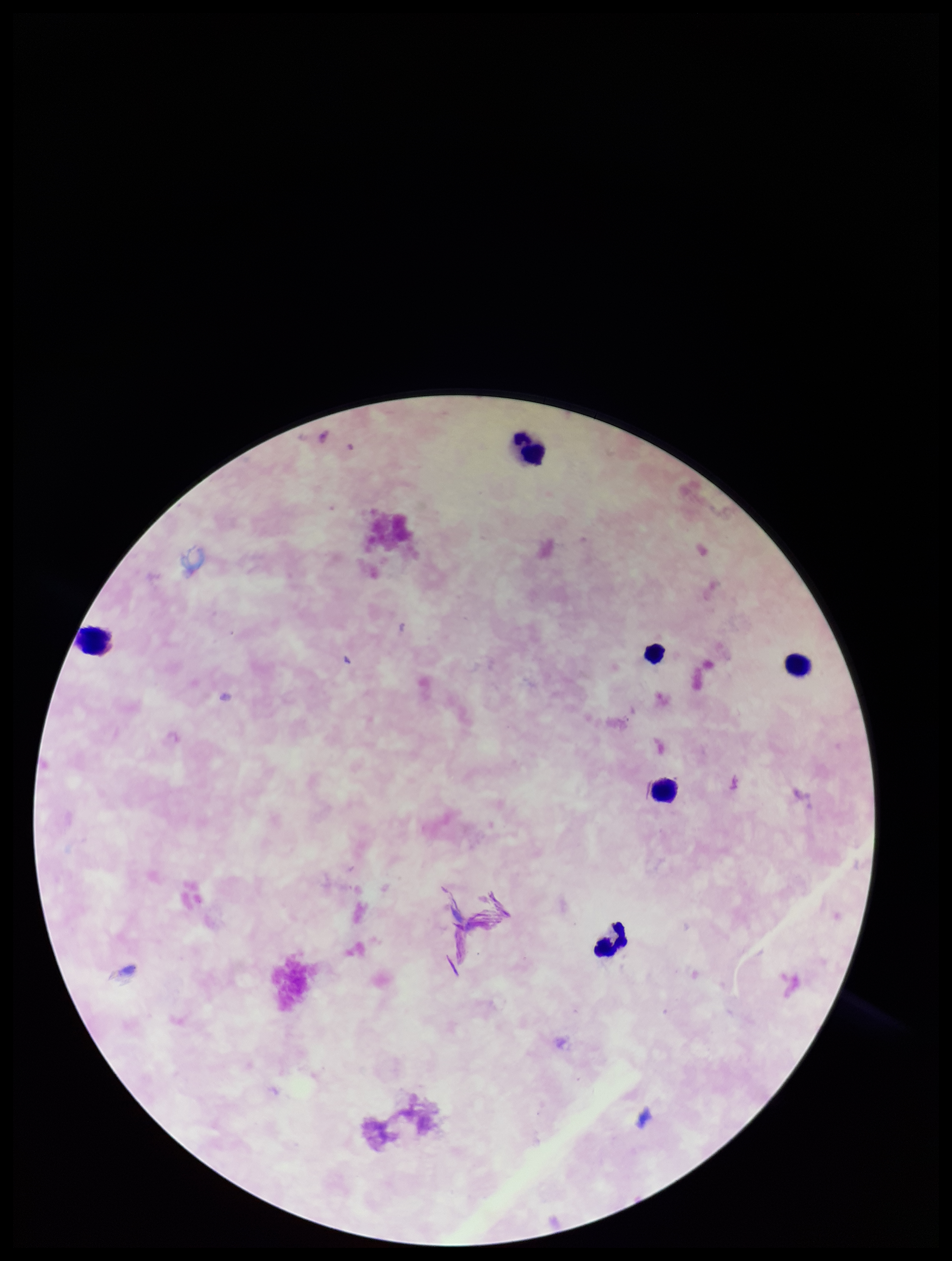

{
  "image_size": "952×1261 pixels",
  "field_of_view": "one from this slide",
  "parasite_count": 0,
  "patient_malaria_status": "negative",
  "capture": "smartphone photograph through the microscope eyepiece",
  "preparation": "thick",
  "stain": "Giemsa",
  "plasmodium_parasites": "none identified",
  "leukocyte_count": 6
}